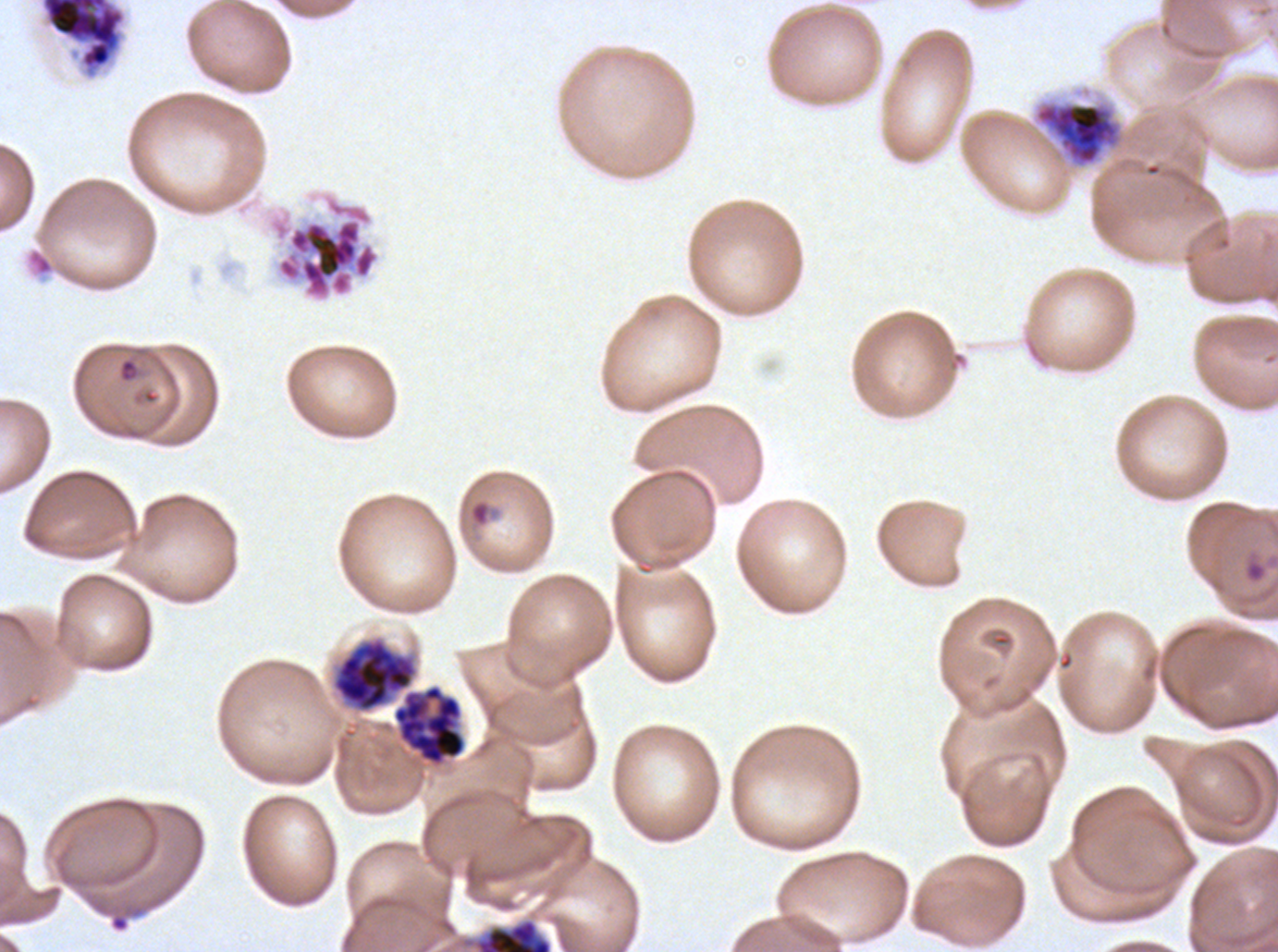

notation = approximate bounding boxes as (x1, y1, x2, y2) in pixels
debris locations = (26, 248, 55, 277)
segmenter locations = (1034, 101, 1123, 168), (266, 190, 381, 303), (331, 637, 466, 765) (two touching objects share this one region)
ring locations = (118, 358, 138, 383), (467, 497, 499, 529), (1245, 560, 1266, 582)
early schizont locations = (42, 0, 124, 69), (331, 637, 466, 765), (475, 919, 552, 951)
field of view = one sub-image of a larger composite
specimen = ex-vivo P. falciparum culture from a patient in The Gambia, grown for 24 to 48 hours
image size = 1278×952 pixels
life-cycle stages observed = ring, early schizont, segmenter
preparation = thin blood smear
stain = Giemsa